Identify the cell.
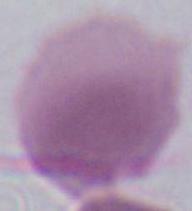
This is an erythrocyte.

magnification = 1000x
modality = photomicrograph